Outline each Trypanosoma brucei.
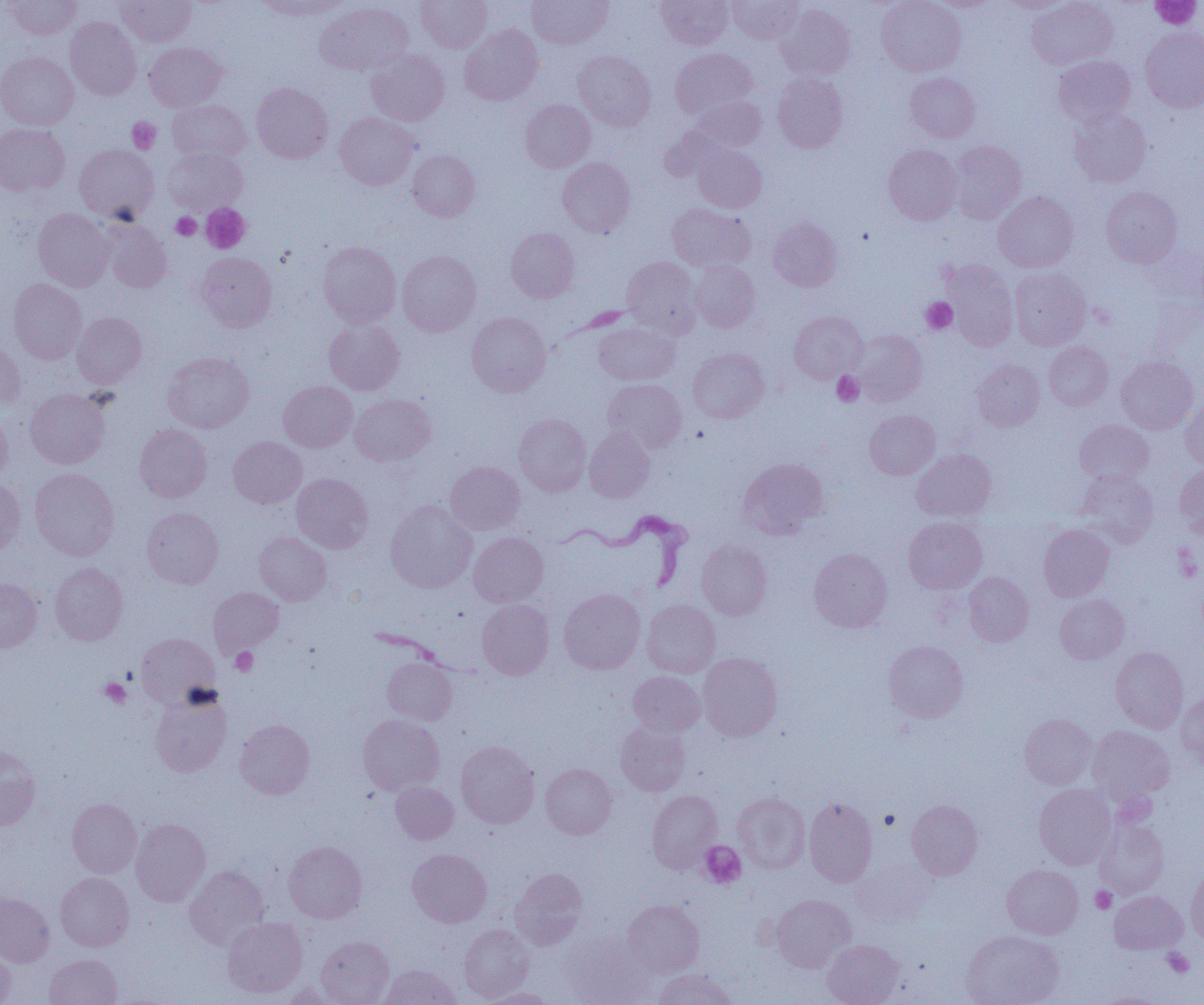

Approximate bounding boxes as (x1,y1)-(x2,y2) corner pairs in pixels.
Trypanosoma brucei: (547,511)-(693,593).

Platelet locations: (1152,0)-(1201,29), (128,117)-(161,153), (200,203)-(251,254), (171,213)-(201,240), (921,297)-(957,334), (832,372)-(864,406), (1174,547)-(1202,582), (230,647)-(258,676), (99,677)-(131,708), (699,841)-(746,888), (1091,887)-(1116,913), (1163,948)-(1194,977). Uninfected red blood cell locations: (4,0)-(82,39), (116,0)-(196,47), (253,0)-(349,20), (416,0)-(492,52), (526,0)-(614,49), (657,0)-(733,49), (729,0)-(803,44), (876,0)-(966,76), (1027,0)-(1118,70), (929,1)-(998,12), (997,1)-(1076,14), (314,2)-(414,75), (777,3)-(856,80), (65,17)-(142,100), (459,24)-(543,105), (1140,27)-(1204,113), (144,42)-(227,111), (366,48)-(450,126), (671,48)-(756,120), (573,50)-(656,131), (0,52)-(78,131), (1053,55)-(1135,126), (772,72)-(848,153), (905,73)-(980,143), (251,82)-(333,164), (688,95)-(767,152), (520,99)-(595,172), (168,100)-(251,164), (1069,107)-(1151,187), (334,112)-(419,189), (0,123)-(69,196), (948,141)-(1027,223), (74,144)-(159,222), (692,145)-(767,213), (883,145)-(962,225), (164,147)-(248,215), (407,150)-(480,221), (557,157)-(635,238), (1101,186)-(1182,268), (993,191)-(1078,272), (667,203)-(755,272), (33,208)-(113,291), (768,217)-(842,292), (99,218)-(172,293), (506,227)-(579,303), (318,241)-(401,328), (397,250)-(482,337), (196,252)-(277,332), (621,256)-(702,336), (690,261)-(760,332), (942,261)-(1019,351), (1009,266)-(1091,350), (8,279)-(87,364), (789,311)-(867,383), (71,312)-(147,388), (467,312)-(551,397), (324,319)-(405,396), (593,322)-(679,385), (852,330)-(927,405), (0,338)-(24,410), (1044,341)-(1113,410), (687,348)-(769,423), (162,352)-(254,433), (1116,356)-(1198,434), (973,359)-(1045,431), (603,379)-(687,453), (278,380)-(357,452), (25,389)-(110,468), (350,394)-(436,466), (1181,398)-(1204,470), (0,407)-(12,484), (865,410)-(940,479), (513,414)-(591,496), (1075,420)-(1153,485), (135,423)-(212,502), (583,428)-(655,502), (228,436)-(307,508), (912,449)-(996,522), (737,457)-(829,540), (445,461)-(525,534), (1175,464)-(1204,539), (30,468)-(119,560), (1077,470)-(1159,547), (291,473)-(373,553), (0,479)-(25,559), (385,501)-(477,593), (142,507)-(223,589), (904,517)-(987,593), (1038,524)-(1114,601), (254,532)-(332,606), (468,533)-(548,607), (696,539)-(772,620), (809,548)-(893,632), (50,561)-(128,645), (964,572)-(1034,646), (0,578)-(42,652), (208,587)-(283,657), (558,588)-(646,674), (1055,594)-(1130,664), (477,599)-(554,679), (641,600)-(721,677), (136,633)-(219,708), (884,641)-(968,723), (1111,647)-(1188,733), (697,653)-(782,741), (382,657)-(457,725), (628,671)-(705,737), (150,690)-(232,776), (1176,693)-(1204,768), (1019,713)-(1097,789), (358,714)-(445,795), (235,719)-(315,799), (615,723)-(690,796), (1088,725)-(1175,803), (456,741)-(540,828), (0,745)-(41,831), (540,763)-(617,839), (390,781)-(459,845), (1034,784)-(1116,869), (647,790)-(722,873), (733,792)-(810,873), (804,797)-(878,886), (67,798)-(141,878), (907,799)-(982,880), (130,818)-(210,906), (1094,819)-(1169,898), (283,841)-(366,923), (407,848)-(492,928), (851,858)-(937,926), (1002,864)-(1083,939), (1186,865)-(1204,944), (184,866)-(269,949), (509,868)-(588,949), (55,872)-(134,951), (1109,891)-(1187,954), (0,892)-(54,967), (771,894)-(855,972), (623,900)-(705,977), (222,917)-(307,998), (459,924)-(534,1002), (961,930)-(1063,1005), (561,931)-(657,1005), (316,936)-(394,1005), (822,939)-(904,1005), (0,942)-(16,1004), (44,954)-(122,1005), (380,964)-(461,1005), (652,969)-(737,1005), (277,981)-(344,1004), (480,987)-(559,1005). Slide-level diagnosis: Trypanosoma brucei. Thin blood film. Captured at 1000x magnification. Image is 1204×1005 pixels. Single field of view. Light microscopy.